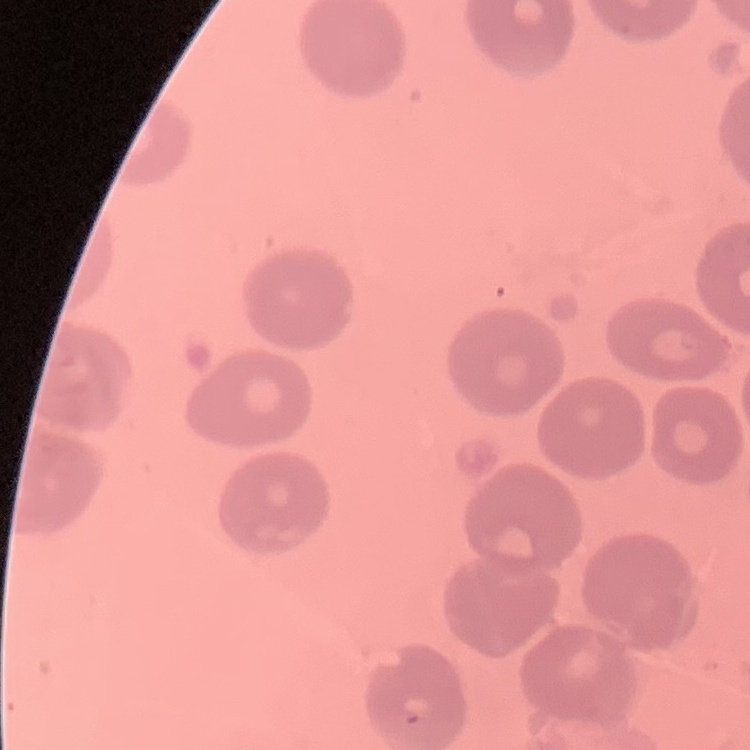
Summary:
  - Erythrocyte morphology: no rouleaux formation
  - Image type: one tile cut from a larger photomicrograph
  - Stain: Field's or Giemsa
  - Preparation: thin peripheral smear